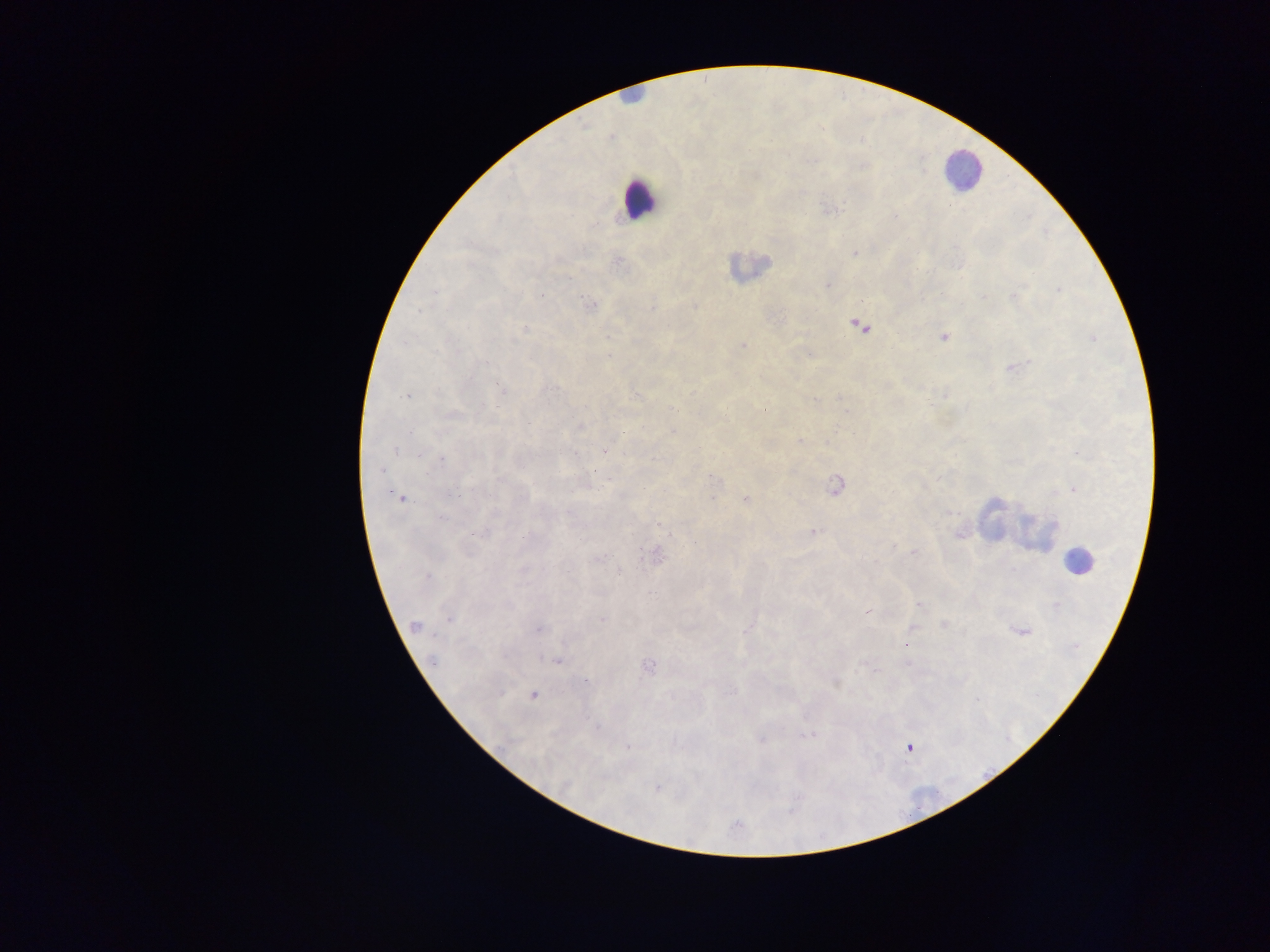

Approximate centers as [x, y] in pixels.
Summary:
  - Leukocyte locations: [960, 168], [638, 200], [751, 266], [996, 516], [1018, 527], [1077, 561]
  - Malaria parasite locations: [755, 175], [802, 191], [829, 210], [595, 225], [855, 253], [617, 262], [960, 266], [570, 278], [827, 285], [1059, 290], [434, 292], [541, 295], [1014, 295], [983, 296], [592, 304], [651, 307], [695, 307], [418, 311], [857, 324], [525, 328], [943, 337], [1093, 339], [743, 346], [810, 355], [609, 356], [484, 362], [1014, 367], [549, 388], [501, 390], [635, 395], [943, 395], [407, 396], [838, 397], [813, 399], [841, 400], [581, 427], [673, 432], [410, 433], [852, 433], [800, 442], [396, 450], [604, 451], [1077, 453], [418, 454], [442, 460], [381, 470], [610, 478], [715, 479], [835, 486], [1074, 489], [454, 494], [401, 497], [712, 498], [745, 499], [568, 512], [951, 513], [440, 517], [658, 524], [812, 532], [481, 534], [959, 534], [695, 541], [892, 546], [913, 553], [655, 555], [599, 558], [619, 572], [427, 577], [920, 603], [1056, 605], [508, 606], [867, 611], [449, 619], [602, 620], [944, 625], [415, 627], [539, 629], [746, 629], [912, 629], [1020, 632], [908, 645], [433, 660], [558, 660], [907, 664], [647, 667], [836, 682], [733, 691], [533, 695], [597, 726], [808, 736], [762, 740], [628, 746], [908, 748], [657, 789], [738, 825]
  - Country: Ghana
  - Field of view: single
  - Capture: mobile-phone photograph through a microscope
  - Image size: 1270×952 pixels
  - Preparation: thick blood film